Assess this cell for malaria.
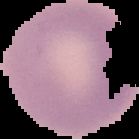
It is uninfected.

From a thin blood film. Image is 139×139 pixels. Segmented cell region on a black background.